Assess this cell for malaria.
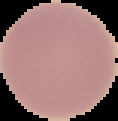

It is uninfected.

preparation: thin blood film
image_size: 118×121 pixels
image_type: segmented cell region on a black background